Assess the morphology of the erythrocytes.
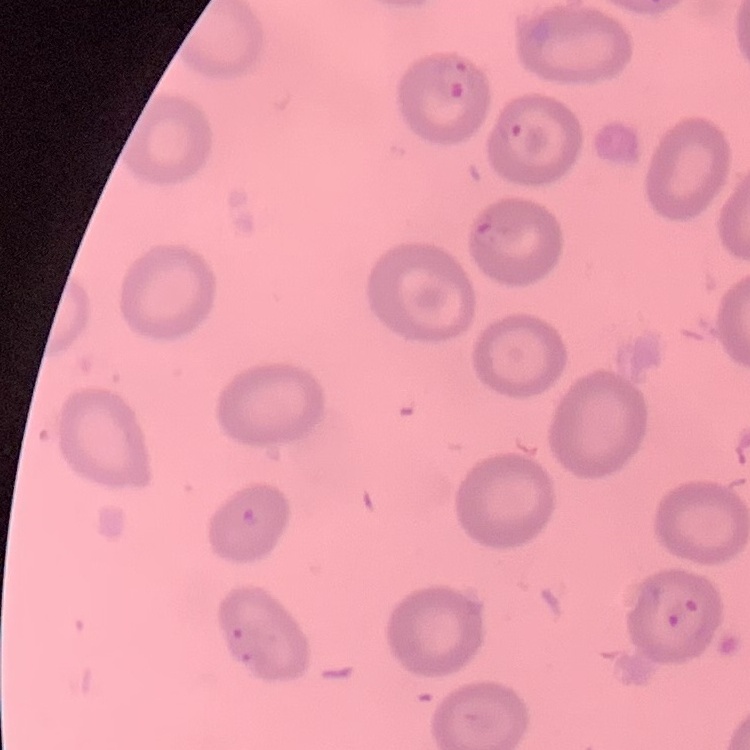
They show no rouleaux formation.

One tile cut from a larger photomicrograph. Thin blood film. Field's or Giemsa stain.